Identify the preparation type.
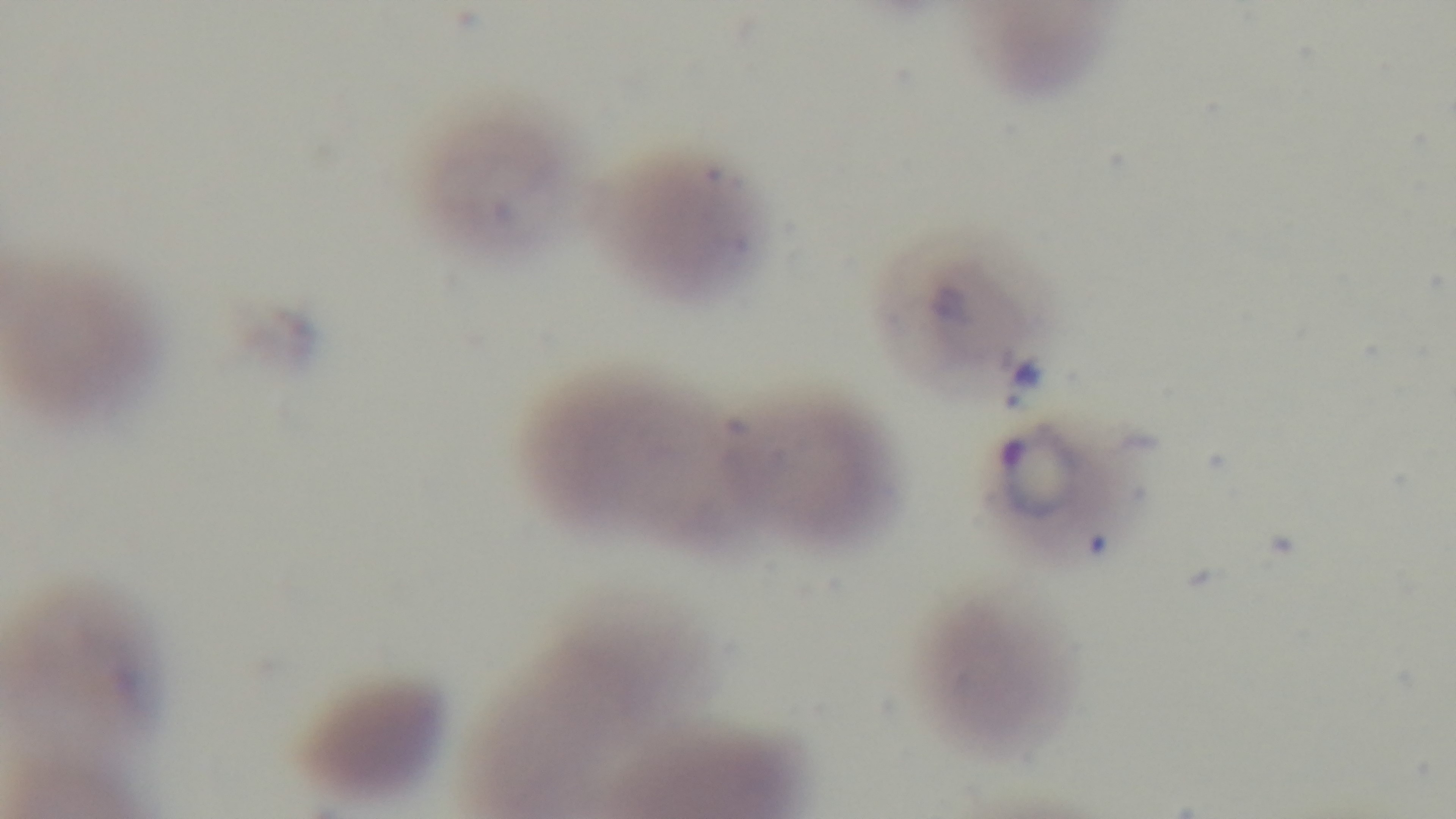
It is a thin blood film.

modality: light microscopy
malaria_status: positive
capture: mounted 4K digital camera
field_of_view: single
objective: 100x oil immersion
stain: Giemsa